Identify the blood parasite species.
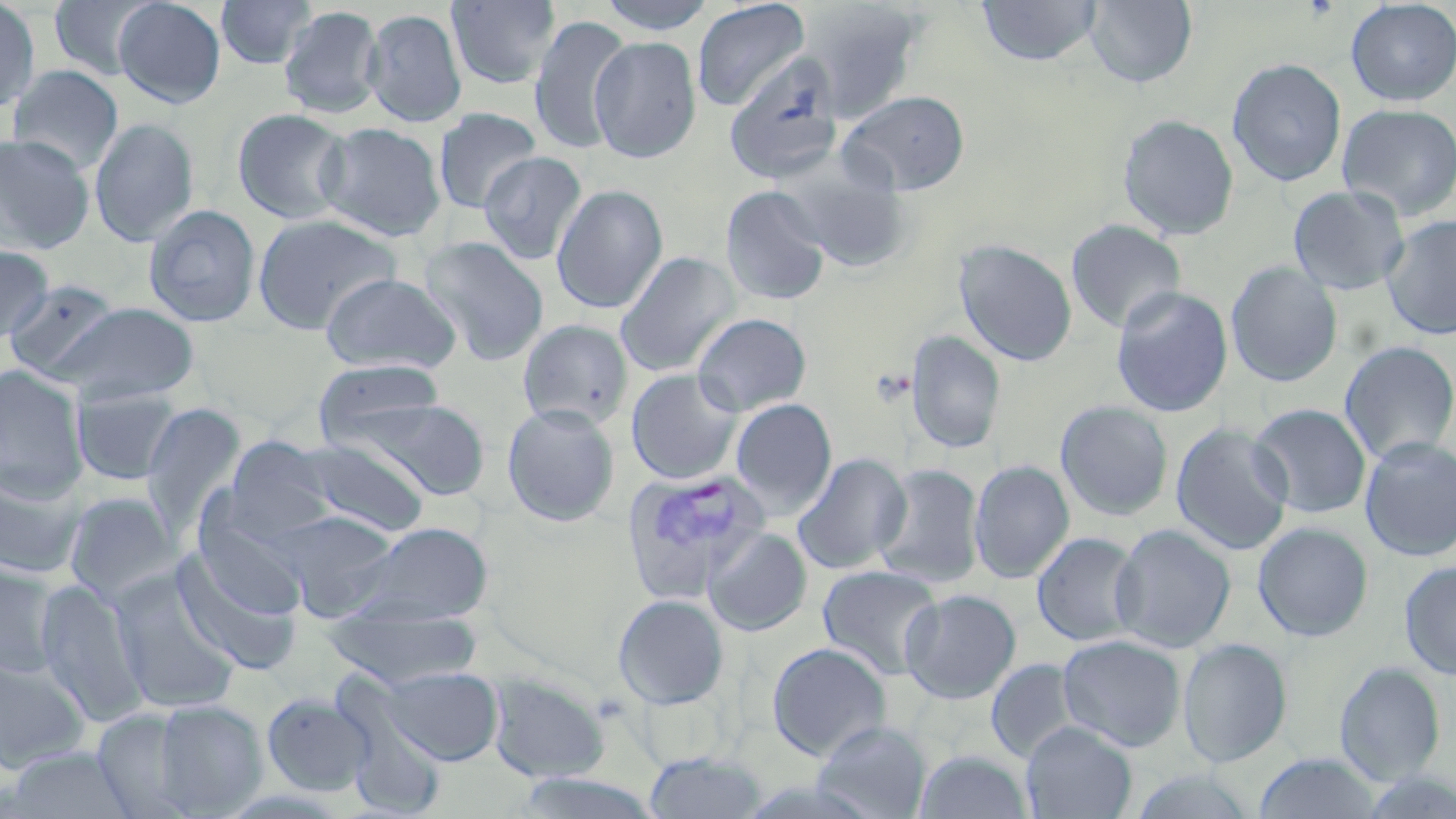
Plasmodium vivax.

Summary:
  - Coordinate format: approximate bounding boxes as (x1,y1)-(x2,y2) corner pairs in pixels
  - Plasmodium vivax-infected red blood cell locations (subset): (621,468)-(772,604)
  - Uninfected red blood cell locations (subset): (49,0)-(160,80), (216,0)-(316,70), (447,0)-(561,89), (597,0)-(717,35), (977,0)-(1103,66), (1084,0)-(1198,87), (0,1)-(40,113), (113,1)-(226,107), (692,1)-(811,112), (795,1)-(927,121), (1345,1)-(1456,106), (278,5)-(385,118), (362,8)-(467,127), (528,14)-(633,156), (589,35)-(702,164), (1226,58)-(1347,187), (6,64)-(124,174), (838,90)-(970,196), (1337,102)-(1456,221), (232,108)-(353,225), (433,108)-(543,214), (1117,114)-(1239,241), (89,118)-(199,247), (317,122)-(447,241), (0,134)-(95,254), (478,151)-(587,265), (783,164)-(915,272), (551,184)-(668,313), (1288,185)-(1410,295), (720,186)-(831,306), (144,204)-(261,327), (251,212)-(404,334), (1381,214)-(1456,340), (1066,219)-(1186,334), (419,236)-(550,366), (953,239)-(1077,366), (0,244)-(54,345), (615,252)-(740,377), (1226,261)-(1343,387), (320,272)-(462,375), (4,278)-(123,382), (1110,287)-(1233,418), (50,302)-(200,405), (692,312)-(812,416), (517,319)-(634,430), (905,331)-(1006,454), (1338,340)-(1456,465), (313,359)-(446,447), (0,365)-(89,501), (626,369)-(743,484), (71,386)-(185,486), (344,396)-(491,501), (730,398)-(837,517), (1055,400)-(1174,521), (139,402)-(248,538), (501,403)-(620,526), (1249,403)-(1371,519), (1171,422)-(1293,555), (223,437)-(337,540), (291,437)-(431,539), (1359,437)-(1456,563), (792,453)-(911,575), (969,460)-(1074,584), (873,464)-(984,589), (0,468)-(87,581), (62,491)-(182,608), (194,510)-(309,621), (272,510)-(402,621), (346,521)-(493,626), (1253,522)-(1374,641), (1111,524)-(1236,654), (702,527)-(812,636), (1032,532)-(1143,647), (171,548)-(302,674), (1399,560)-(1456,680), (0,562)-(65,682), (817,565)-(943,680), (110,570)-(243,714), (34,578)-(149,729), (900,589)-(1021,704), (613,595)-(729,709), (323,607)-(483,688), (1058,634)-(1186,752), (1178,638)-(1292,768), (767,642)-(892,761), (0,655)-(93,773), (986,658)-(1084,764), (1334,662)-(1445,785), (381,666)-(504,766), (487,672)-(610,783), (332,678)-(449,818), (261,693)-(374,797), (146,699)-(269,816), (91,707)-(203,817), (814,720)-(931,819), (1022,722)-(1137,818), (3,746)-(141,819), (915,749)-(1031,818), (642,751)-(768,818), (1252,752)-(1382,818), (1125,769)-(1260,818), (511,771)-(665,818)
  - Modality: optical microscopy
  - Image size: 1456×819 pixels
  - Field of view: single
  - Magnification: 1000x
  - Stain: May-Grünwald-Giemsa
  - Preparation: thin blood film